Give the preparation type.
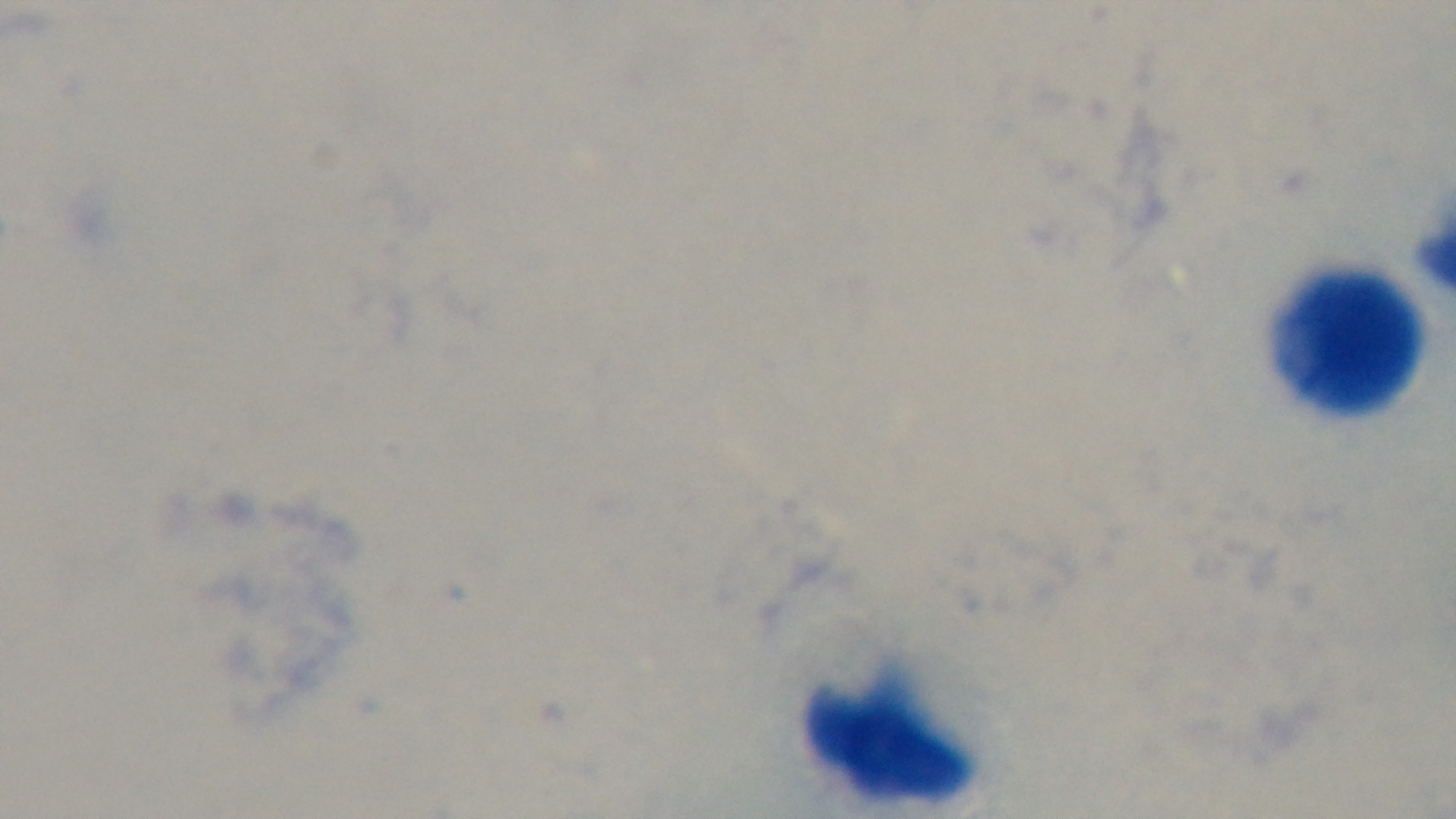

A thick smear.

Summary:
  - Objective: 100x oil immersion
  - Stain: Giemsa
  - Modality: light microscopy
  - Capture: mounted 4K digital camera
  - Field of view: one from the slide
  - Malaria status: uninfected